Classify this cell by malaria status.
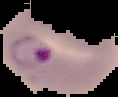

Parasitized.

Summary:
  - Image type: cell region segmented out of the field of view; surrounding area masked to black
  - Image size: 118×97 pixels
  - Preparation: thin blood smear